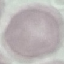

Result: negative for malaria parasites. Automatically extracted cell patch, resized to 64 × 64 pixels. Thin blood film. Acquired by smartphone through the microscope eyepiece. Giemsa-stained preparation.